Report the malaria status of this cell.
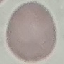
Uninfected.

Summary:
  - Capture: smartphone camera at the microscope eyepiece
  - Image type: cell patch, automatically extracted from a larger field of view and resized to 64 × 64 pixels
  - Preparation: thin blood film
  - Stain: Giemsa